Identify the parasite.
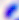
This is Toxoplasma gondii.

magnification = 400x
modality = micrograph